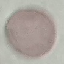
malaria status = uninfected
capture = smartphone through the microscope eyepiece
image type = automatically extracted cell patch, resized to 64 × 64 pixels
stain = Giemsa
preparation = thin smear